Assess the morphology of the red blood cells.
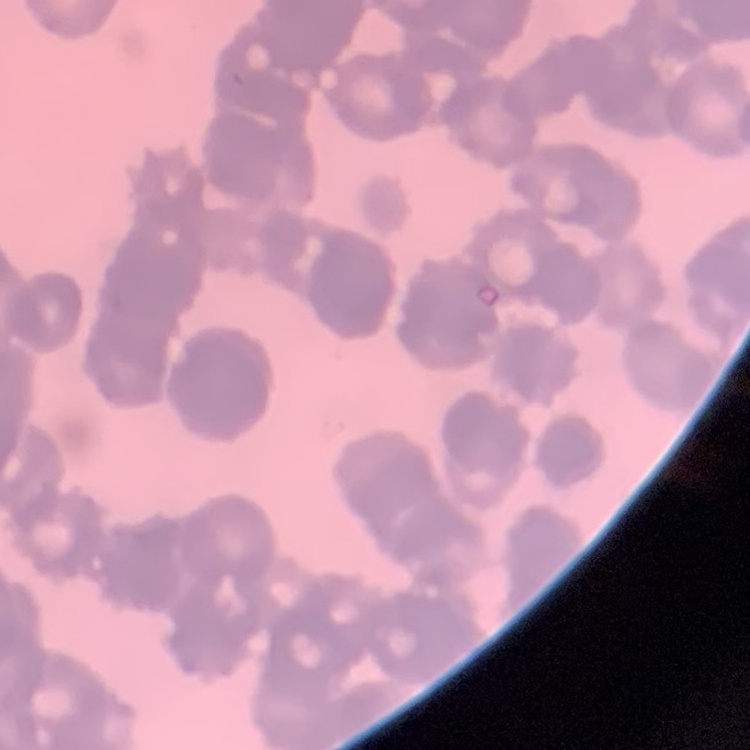

Rouleaux formation.

Summary:
  - Preparation: thin blood smear
  - Image type: one tile cut from a larger photomicrograph
  - Stain: Field's or Giemsa